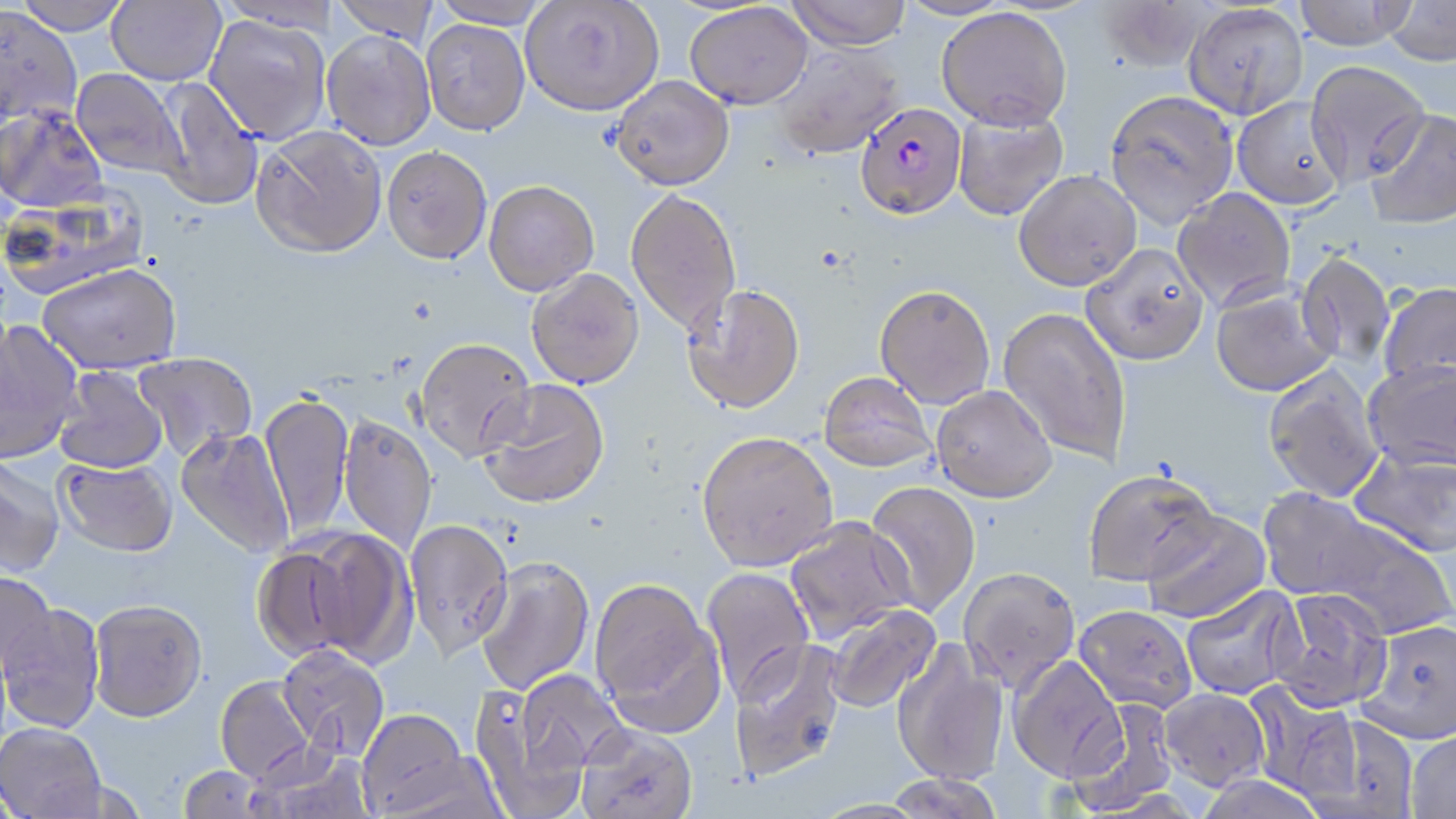

Summary:
  - Coordinate format: approximate bounding boxes as named x1/y1/x2/y2 corners in pixels
  - Plasmodium falciparum-infected red blood cell locations: (x1=853, y1=102, x2=968, y2=221)
  - Uninfected red blood cell locations: (x1=12, y1=0, x2=133, y2=35), (x1=106, y1=0, x2=226, y2=86), (x1=332, y1=0, x2=442, y2=43), (x1=430, y1=0, x2=551, y2=29), (x1=785, y1=0, x2=912, y2=51), (x1=1292, y1=0, x2=1419, y2=51), (x1=520, y1=1, x2=664, y2=116), (x1=1096, y1=1, x2=1215, y2=72), (x1=1382, y1=1, x2=1456, y2=66), (x1=684, y1=3, x2=813, y2=109), (x1=1182, y1=4, x2=1309, y2=119), (x1=0, y1=6, x2=82, y2=127), (x1=936, y1=8, x2=1072, y2=130), (x1=203, y1=14, x2=332, y2=143), (x1=421, y1=18, x2=531, y2=136), (x1=321, y1=30, x2=436, y2=151), (x1=770, y1=43, x2=904, y2=160), (x1=1305, y1=60, x2=1431, y2=186), (x1=71, y1=68, x2=188, y2=179), (x1=610, y1=76, x2=734, y2=191), (x1=153, y1=77, x2=263, y2=211), (x1=1104, y1=89, x2=1239, y2=228), (x1=1232, y1=97, x2=1347, y2=210), (x1=0, y1=105, x2=108, y2=214), (x1=952, y1=106, x2=1069, y2=222), (x1=1364, y1=109, x2=1456, y2=229), (x1=250, y1=126, x2=387, y2=260), (x1=381, y1=146, x2=492, y2=266), (x1=1013, y1=170, x2=1141, y2=292), (x1=483, y1=180, x2=600, y2=297), (x1=1172, y1=188, x2=1297, y2=311), (x1=625, y1=189, x2=741, y2=336), (x1=1080, y1=244, x2=1209, y2=367), (x1=1296, y1=252, x2=1396, y2=371), (x1=37, y1=264, x2=182, y2=376), (x1=526, y1=269, x2=645, y2=390), (x1=1378, y1=282, x2=1456, y2=393), (x1=681, y1=285, x2=806, y2=416), (x1=874, y1=286, x2=995, y2=410), (x1=1210, y1=286, x2=1336, y2=398), (x1=997, y1=307, x2=1132, y2=465), (x1=0, y1=320, x2=83, y2=464), (x1=414, y1=339, x2=536, y2=464), (x1=133, y1=352, x2=257, y2=461), (x1=1362, y1=363, x2=1456, y2=475), (x1=53, y1=366, x2=168, y2=475), (x1=1262, y1=366, x2=1385, y2=504), (x1=818, y1=373, x2=935, y2=475), (x1=478, y1=381, x2=611, y2=511), (x1=930, y1=387, x2=1056, y2=505), (x1=260, y1=391, x2=354, y2=540), (x1=338, y1=416, x2=437, y2=552), (x1=175, y1=428, x2=294, y2=559), (x1=696, y1=435, x2=838, y2=574), (x1=1348, y1=449, x2=1456, y2=560), (x1=0, y1=455, x2=66, y2=578), (x1=54, y1=458, x2=177, y2=559), (x1=1084, y1=472, x2=1218, y2=589), (x1=864, y1=483, x2=980, y2=618), (x1=1255, y1=490, x2=1395, y2=609), (x1=1142, y1=511, x2=1272, y2=625), (x1=1300, y1=513, x2=1456, y2=641), (x1=783, y1=518, x2=913, y2=643), (x1=404, y1=519, x2=514, y2=663), (x1=285, y1=528, x2=415, y2=668), (x1=253, y1=545, x2=367, y2=664), (x1=476, y1=558, x2=595, y2=695), (x1=702, y1=567, x2=815, y2=706), (x1=957, y1=569, x2=1081, y2=697), (x1=0, y1=570, x2=56, y2=675), (x1=590, y1=580, x2=723, y2=734), (x1=1180, y1=586, x2=1303, y2=700), (x1=1267, y1=590, x2=1393, y2=716), (x1=88, y1=602, x2=207, y2=726), (x1=0, y1=604, x2=105, y2=734), (x1=823, y1=604, x2=943, y2=714), (x1=1073, y1=607, x2=1196, y2=716), (x1=1356, y1=622, x2=1456, y2=747), (x1=729, y1=639, x2=848, y2=784), (x1=890, y1=640, x2=1010, y2=789), (x1=278, y1=646, x2=389, y2=760), (x1=1008, y1=657, x2=1128, y2=787), (x1=514, y1=670, x2=629, y2=782), (x1=215, y1=676, x2=317, y2=786), (x1=469, y1=681, x2=594, y2=819), (x1=1244, y1=682, x2=1362, y2=804), (x1=1159, y1=690, x2=1271, y2=794), (x1=1066, y1=698, x2=1181, y2=815), (x1=356, y1=712, x2=480, y2=817), (x1=1302, y1=712, x2=1420, y2=819), (x1=0, y1=723, x2=107, y2=818), (x1=575, y1=725, x2=698, y2=819), (x1=1405, y1=731, x2=1456, y2=819), (x1=249, y1=748, x2=378, y2=819), (x1=179, y1=766, x2=264, y2=818), (x1=881, y1=774, x2=1004, y2=819), (x1=1195, y1=777, x2=1328, y2=819)
  - Slide-level diagnosis: Plasmodium falciparum
  - Modality: light microscopy
  - Preparation: thin blood smear
  - Field of view: one of a larger specimen
  - Magnification: 1000x
  - Image size: 1456×819 pixels
  - Stain: May-Grünwald-Giemsa